Outline each blood parasite and name the species.
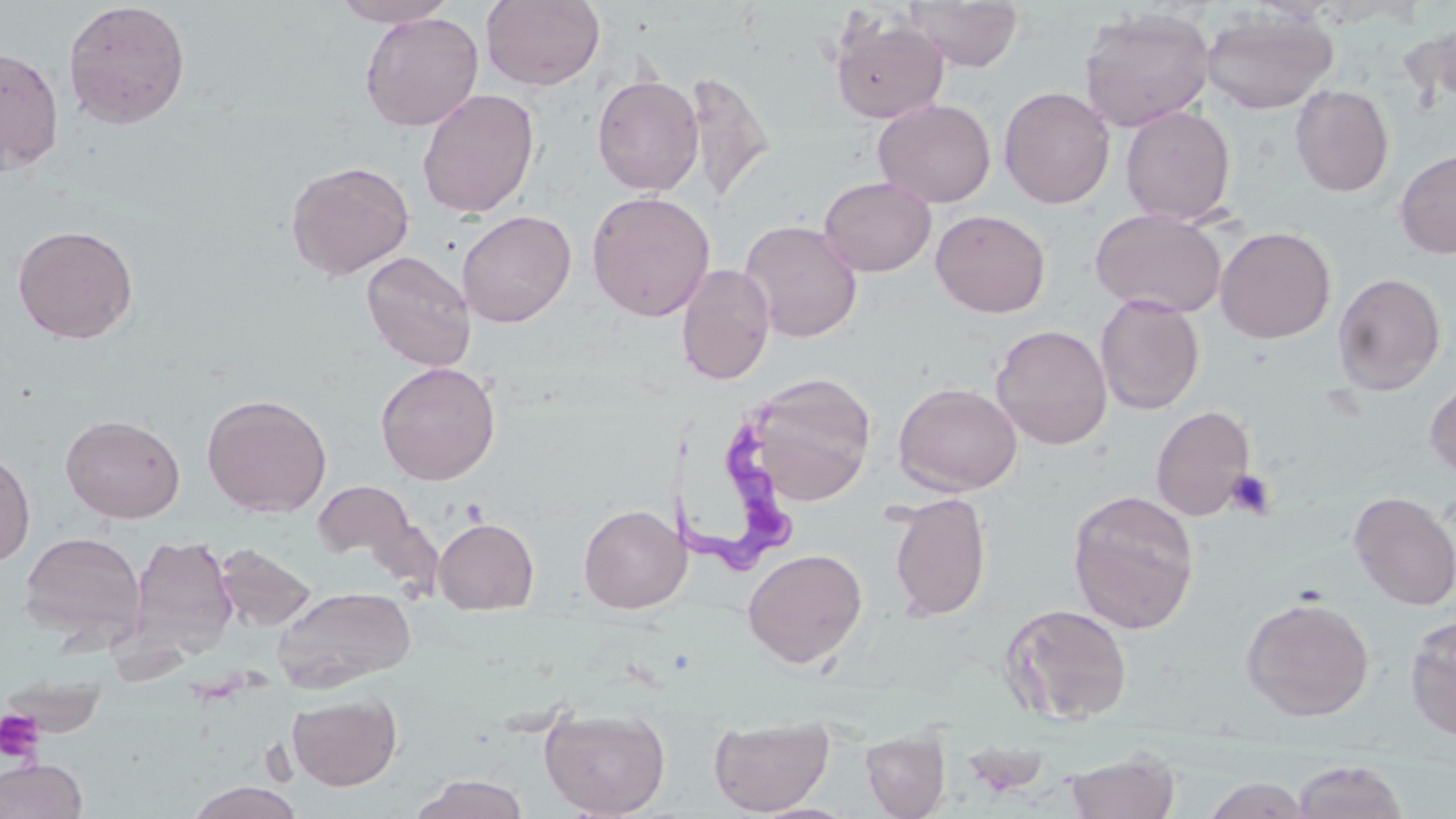

Approximate bounding boxes as (x1, y1, x2, y2) in pixels.
Trypanosoma brucei: (657, 399, 802, 573).
No Plasmodium falciparum, Plasmodium ovale, Plasmodium malariae, Plasmodium vivax, or Babesia divergens observed.

slide-level diagnosis = Trypanosoma brucei
stain = May-Grünwald-Giemsa
magnification = 1000x
preparation = thin blood film
uninfected red blood cell locations = approximate bounding boxes as (x1, y1, x2, y2) in pixels: (329, 0, 459, 27), (481, 0, 606, 91), (903, 0, 1024, 71), (62, 1, 191, 129), (1200, 6, 1338, 115), (1078, 7, 1215, 132), (359, 11, 484, 131), (830, 15, 948, 124), (0, 45, 64, 175), (682, 70, 775, 207), (592, 73, 704, 196), (1290, 84, 1394, 197), (998, 86, 1116, 209), (417, 88, 540, 218), (873, 98, 996, 207), (1120, 105, 1236, 226), (1394, 148, 1456, 259), (285, 160, 414, 281), (819, 176, 936, 276), (587, 190, 715, 322), (1090, 207, 1227, 318), (930, 209, 1050, 318), (457, 210, 576, 327), (739, 219, 863, 343), (12, 223, 138, 344), (1215, 226, 1336, 344), (361, 251, 477, 372), (676, 263, 775, 386), (1331, 271, 1446, 395), (1095, 294, 1204, 415), (991, 324, 1112, 450), (375, 361, 501, 485), (743, 372, 878, 506), (1424, 374, 1456, 482), (893, 381, 1022, 496), (202, 393, 332, 517), (1150, 404, 1256, 521), (60, 414, 185, 523), (0, 447, 35, 568), (311, 479, 417, 562), (1066, 489, 1201, 634), (1348, 491, 1456, 611), (886, 492, 992, 621), (578, 504, 691, 613), (433, 517, 539, 615), (19, 531, 146, 648), (130, 533, 238, 659), (215, 543, 316, 632), (742, 548, 868, 669), (272, 586, 415, 691), (1240, 595, 1376, 721), (1000, 603, 1134, 726), (1405, 617, 1456, 742), (287, 691, 402, 791), (540, 707, 670, 818), (709, 715, 834, 816), (861, 730, 950, 818), (1064, 749, 1180, 819), (0, 758, 88, 819), (1291, 759, 1410, 819), (410, 773, 529, 818), (1200, 776, 1312, 818), (185, 781, 306, 818)
platelet locations = approximate bounding boxes as (x1, y1, x2, y2) in pixels: (0, 708, 45, 764)
image size = 1456×819 pixels
modality = optical microscopy
field of view = single